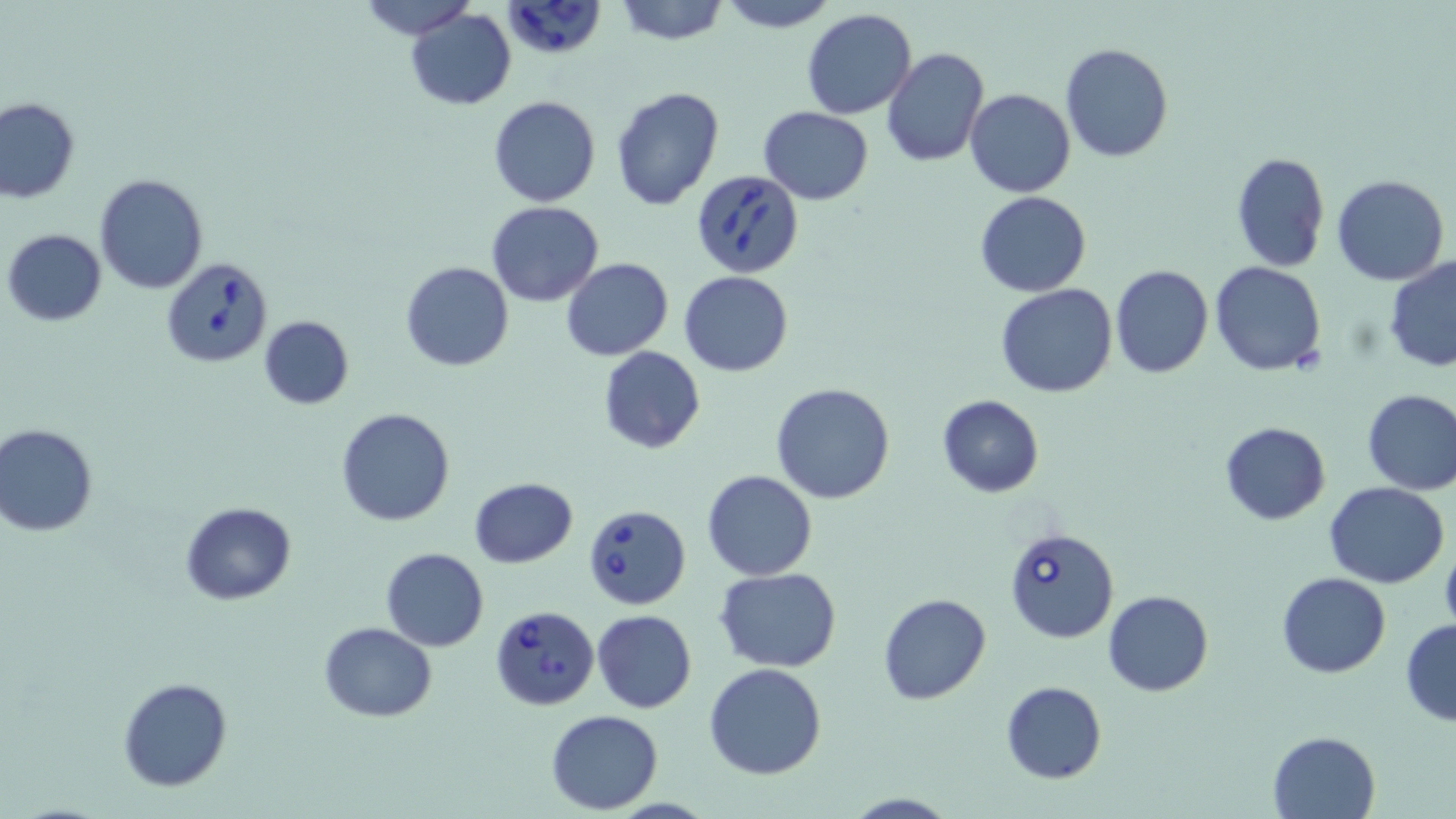
Summary:
  - Coordinate format: approximate bounding boxes as [x1, y1, x2, y2] in pixels
  - Uninfected red blood cell locations: [355, 0, 478, 41], [614, 0, 728, 45], [716, 0, 838, 32], [405, 7, 515, 111], [802, 8, 917, 120], [1060, 42, 1174, 164], [881, 46, 988, 168], [610, 86, 725, 211], [967, 88, 1076, 198], [488, 96, 600, 207], [1, 98, 79, 203], [758, 106, 874, 203], [1230, 152, 1329, 273], [95, 173, 208, 293], [1333, 175, 1450, 286], [974, 192, 1092, 296], [485, 201, 604, 307], [3, 229, 107, 326], [1384, 255, 1456, 372], [560, 257, 673, 361], [400, 261, 514, 372], [1209, 262, 1328, 378], [1111, 265, 1214, 380], [680, 271, 793, 376], [995, 285, 1119, 398], [258, 316, 353, 410], [598, 345, 705, 454], [770, 381, 896, 503], [1360, 388, 1456, 495], [937, 394, 1044, 496], [335, 408, 456, 527], [1220, 422, 1329, 525], [0, 425, 99, 535], [702, 469, 817, 582], [469, 478, 578, 568], [1325, 482, 1449, 587], [179, 502, 297, 605], [380, 547, 488, 651], [716, 566, 840, 673], [1276, 572, 1389, 677], [1103, 590, 1214, 696], [879, 593, 992, 705], [591, 609, 696, 713], [1399, 617, 1456, 727], [318, 621, 437, 722], [703, 664, 828, 780], [118, 676, 233, 792], [1001, 681, 1106, 784], [545, 710, 665, 814], [1267, 730, 1381, 818], [842, 793, 961, 819]
  - Babesia divergens-infected red blood cell locations: [507, 1, 607, 61], [692, 168, 807, 277], [160, 256, 273, 367], [585, 504, 692, 610], [1004, 525, 1121, 643], [489, 604, 599, 712]
  - Slide-level diagnosis: Babesia divergens
  - Modality: light microscopy
  - Preparation: thin blood film
  - Image size: 1456×819 pixels
  - Field of view: single
  - Magnification: 1000x
  - Stain: May-Grünwald-Giemsa